Outline every malaria parasite.
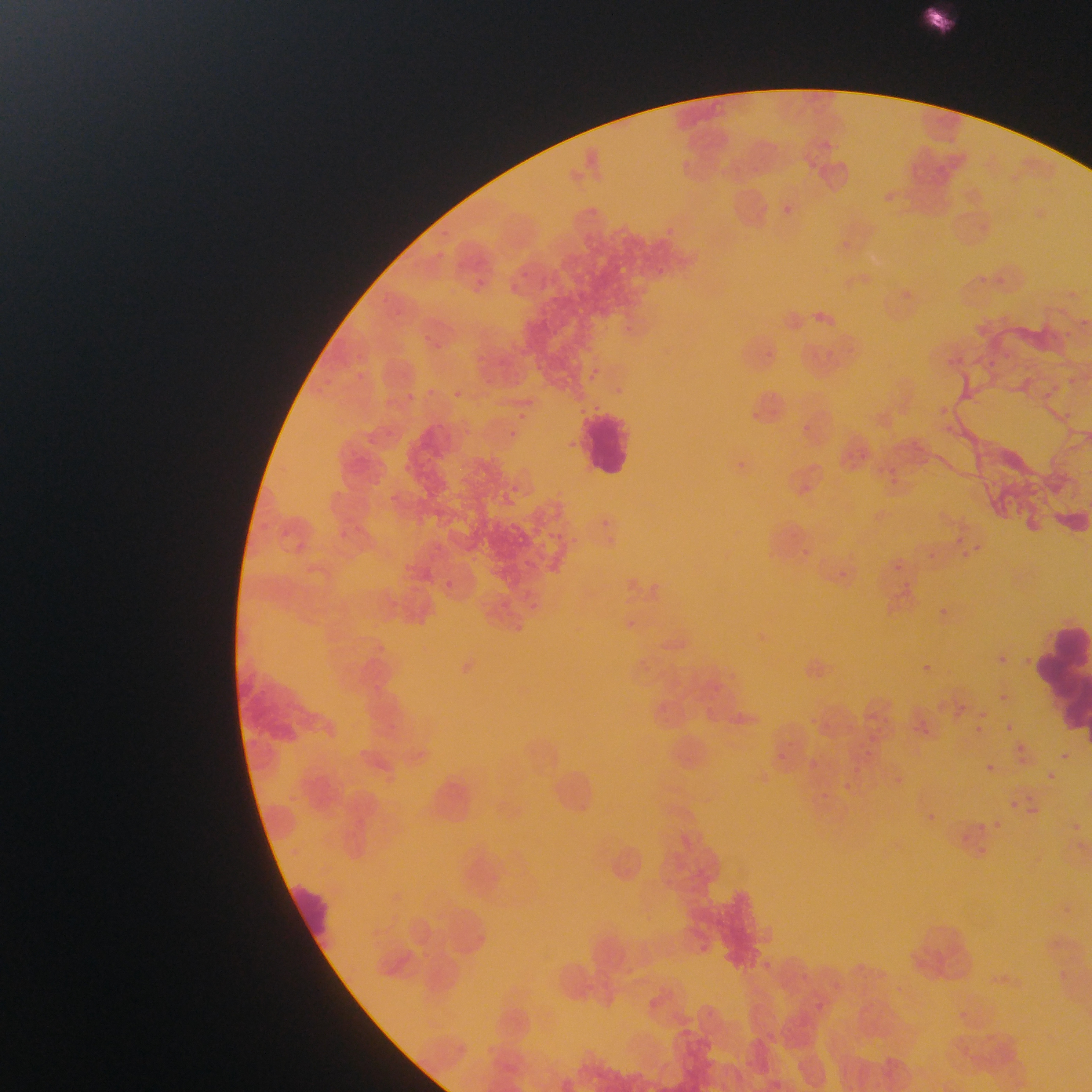
Approximate bounding boxes as left top right bottom in pixels.
Malaria parasites: 582 366 597 381; 616 383 628 396; 452 387 469 404; 401 390 428 409; 513 409 531 424; 505 431 517 436; 564 434 575 443; 508 478 525 491; 522 598 540 611; 933 604 952 622; 993 649 1018 673; 1024 653 1035 663; 920 659 938 672; 997 689 1027 706; 926 698 955 716; 958 698 968 711; 1004 719 1015 736; 873 721 900 732; 971 722 986 737; 1010 737 1032 765; 860 739 893 752; 1061 745 1079 758; 779 752 795 762; 856 752 869 772; 810 761 820 772; 982 761 997 775; 1041 772 1058 789; 837 776 861 806; 1008 797 1022 810; 1072 816 1088 836 | approximate x y pixel centers of objects too small to bound: 447 579.

Leukocyte locations: 915 4 957 37; 579 411 635 476; 1043 622 1089 726; 282 876 339 952; 905 915 981 987. Image is 1092×1092 pixels. Thin blood film. Collected in Ghana. Photographed through a microscope with a mobile-phone camera. Single field of view.